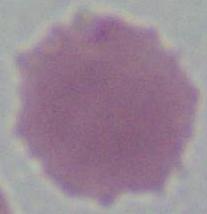

Summary:
  - Magnification: 1000x
  - Modality: photomicrograph
  - Identification: red blood cell